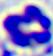
modality = micrograph
magnification = 400x
identification = leukocyte